Describe the morphology of the red blood cells.
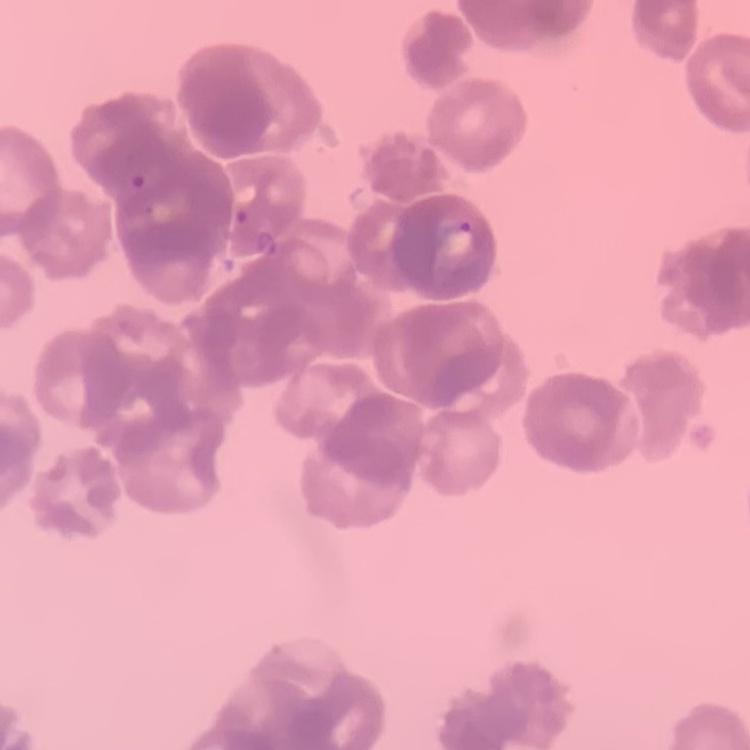

Rouleaux formation.

Thin blood film. Field's or Giemsa stain. Square crop of a larger photomicrograph.